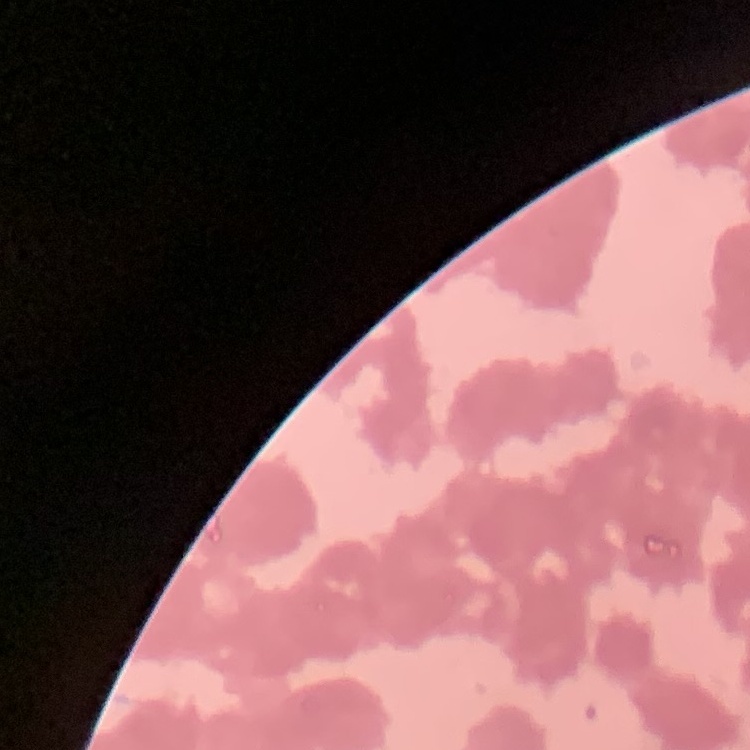

{
  "erythrocyte_morphology": "rouleaux formation",
  "preparation": "thin blood smear",
  "stain": "Field's or Giemsa",
  "image_type": "one tile cut from a larger photomicrograph"
}